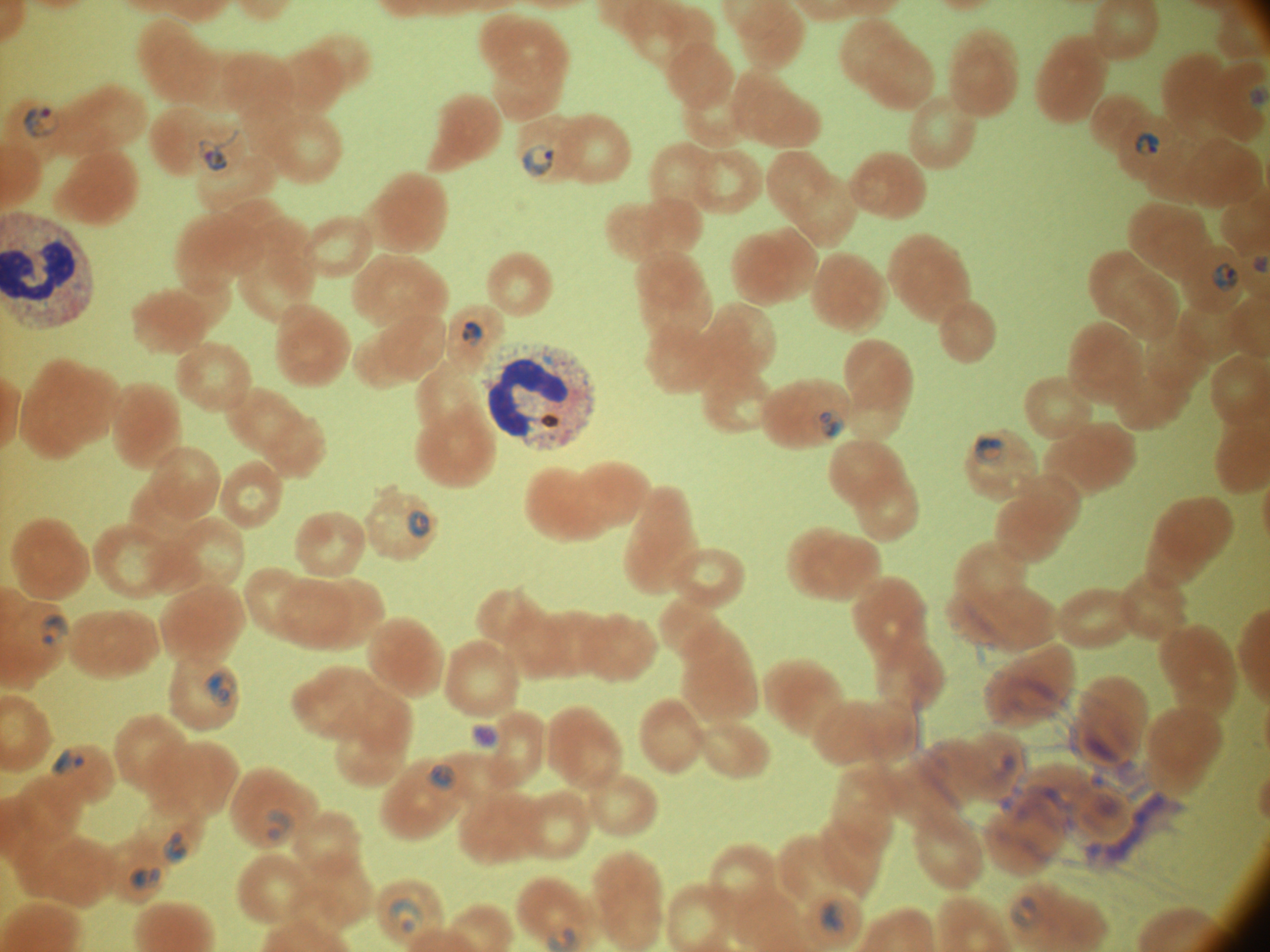
Approximate bounding boxes as (x1,y1)-(x2,y2) corner pairs in pixels, from the source annotation, which is not necessarily exhaustive. Ring form locations: (1248,86)-(1269,103), (23,104)-(60,141), (196,129)-(239,173), (1135,130)-(1161,157), (521,143)-(556,178), (1252,256)-(1269,274), (1210,262)-(1239,293), (460,320)-(483,347), (815,407)-(846,440), (974,433)-(1009,465), (407,509)-(431,538), (40,613)-(70,644), (203,668)-(237,707), (470,722)-(500,748), (51,747)-(85,777), (426,764)-(456,790), (267,808)-(292,840), (162,830)-(188,864), (129,865)-(163,890), (1010,895)-(1040,928), (389,897)-(425,933), (819,900)-(847,932). Image is 1270×952 pixels. Giemsa-stained preparation. Species: Plasmodium falciparum. Thin blood smear. Captured at 100x magnification. Leica DM2000 optical microscope with a built-in camera. One field from this slide.